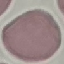

Malaria status: uninfected. Cell patch, automatically extracted from a larger field of view and resized to 64 × 64 pixels. Thin smear of blood. Giemsa-stained preparation. Photographed with a smartphone camera at the microscope eyepiece.